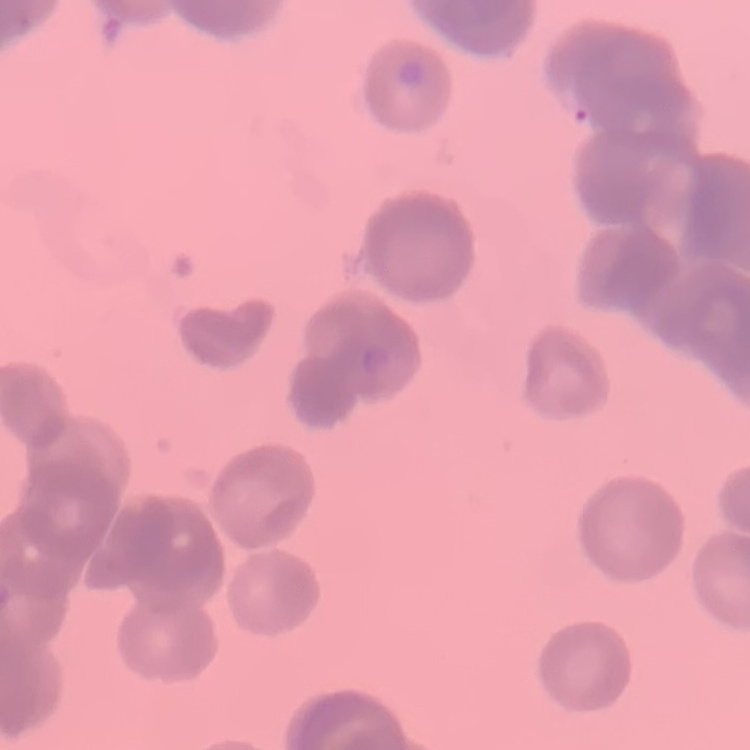
Summary:
  - Red blood cell morphology: rouleaux formation
  - Image type: square crop of a larger photomicrograph
  - Preparation: thin blood smear
  - Stain: Field's or Giemsa